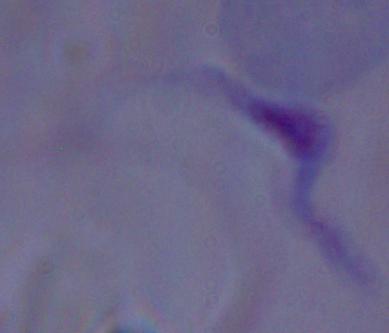

Summary:
  - Modality: micrograph
  - Magnification: 1000x
  - Identification: trypanosome